Identify the preparation type.
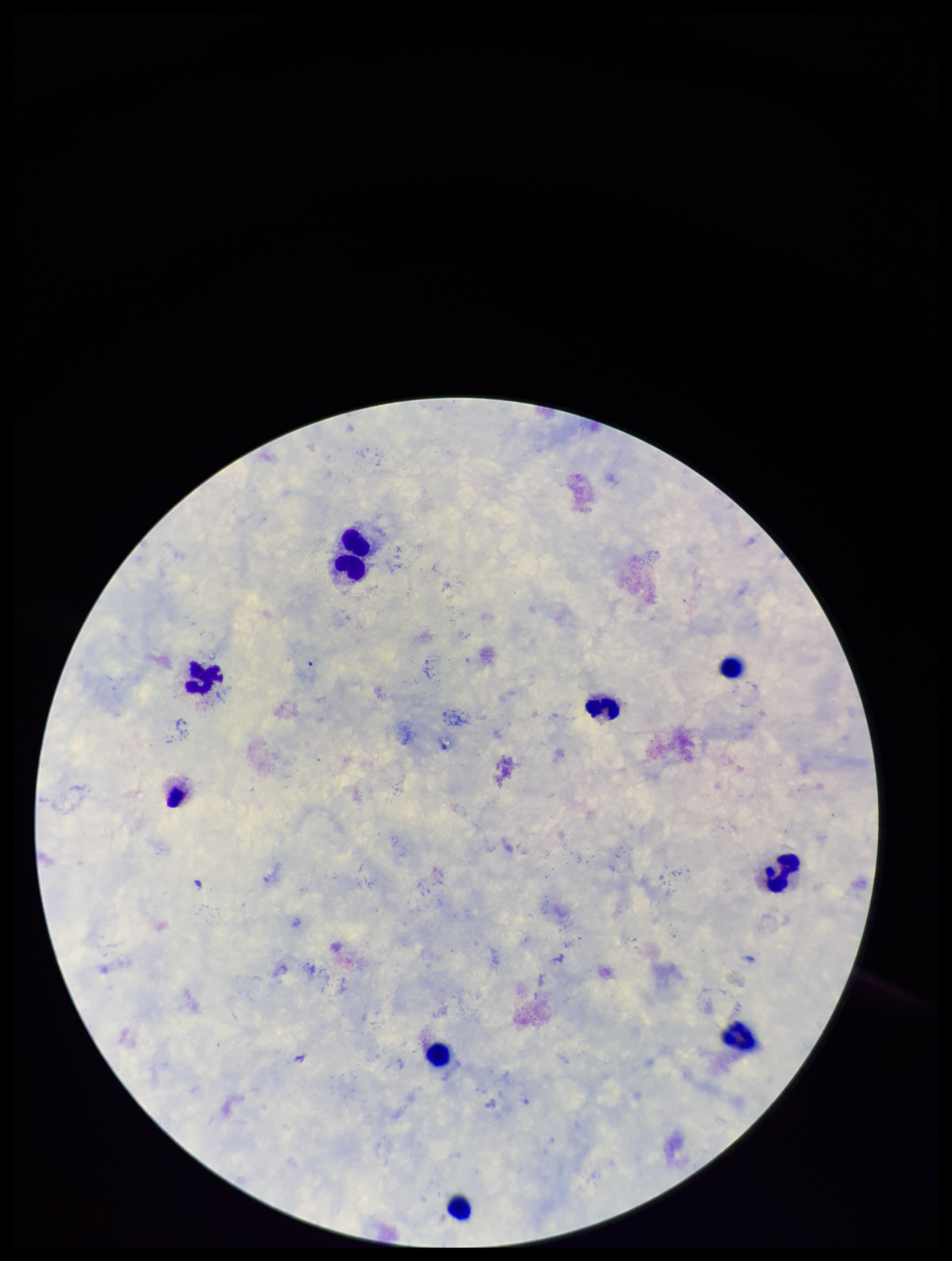

A thick smear.

{
  "stain": "Giemsa",
  "image_size": "952×1261 pixels",
  "leukocyte_count": 10,
  "parasite_count": 0,
  "patient_malaria_status": "negative",
  "plasmodium_parasites": "none identified",
  "field_of_view": "one from this slide",
  "capture": "smartphone photograph through the microscope eyepiece"
}